Identify the parasite.
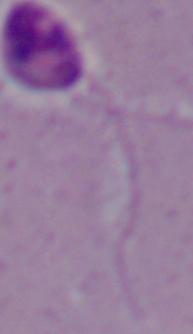
This is Leishmania.

modality = micrograph
magnification = 1000x